Outline each blood parasite and name the species.
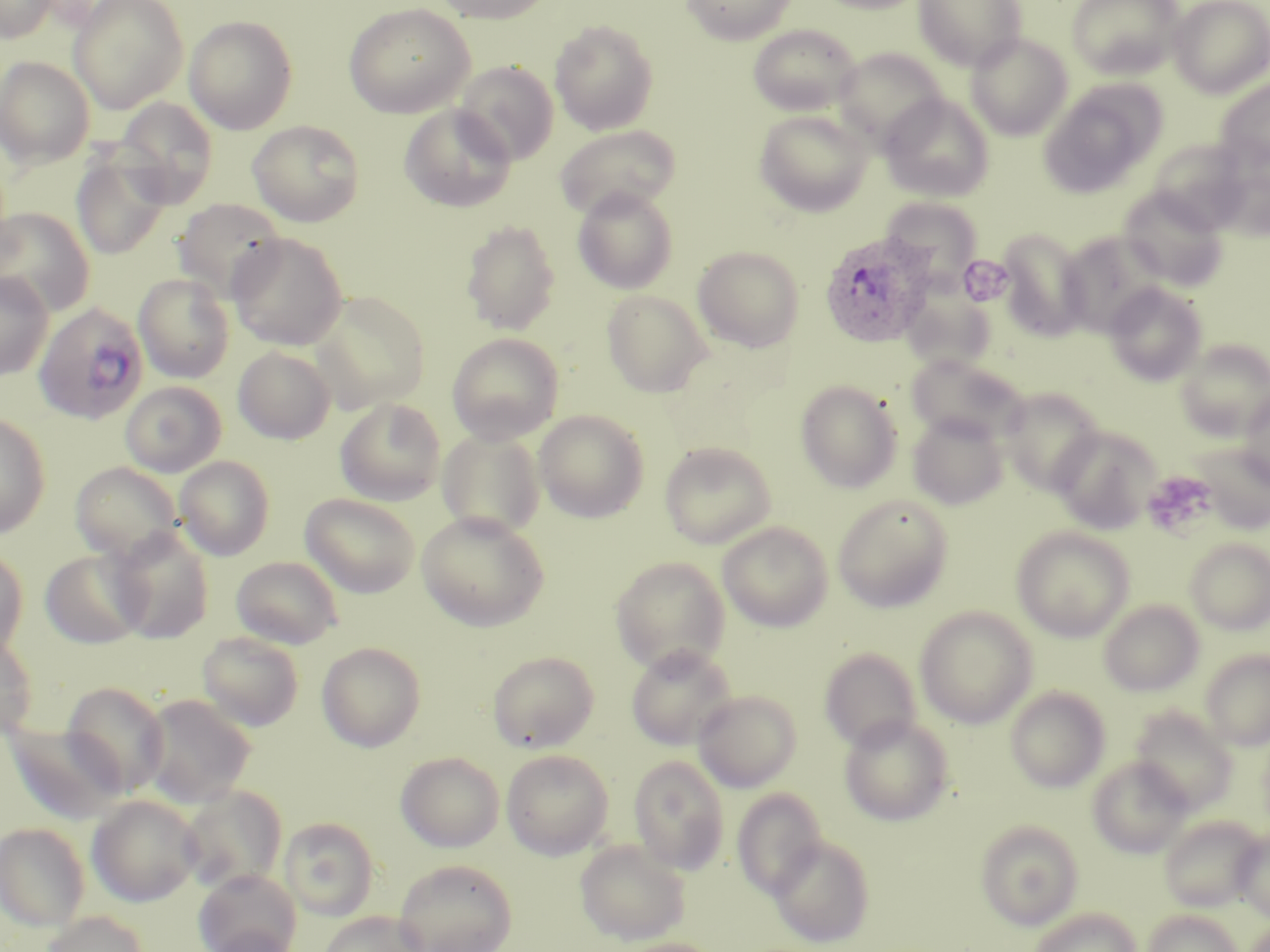

Approximate bounding boxes as (x1, y1, x2, y2) in pixels.
Plasmodium ovale-infected red blood cells: (819, 231, 934, 348), (33, 302, 149, 425).
No Plasmodium falciparum, Plasmodium malariae, Plasmodium vivax, Babesia divergens, or Trypanosoma brucei observed.

Summary:
  - Uninfected red blood cell locations: (0, 0, 57, 42), (69, 0, 188, 113), (432, 0, 557, 25), (680, 0, 797, 45), (812, 0, 930, 14), (912, 0, 1028, 71), (1066, 0, 1184, 81), (1168, 0, 1270, 97), (342, 2, 475, 119), (183, 15, 298, 134), (549, 20, 658, 135), (747, 24, 862, 117), (965, 32, 1073, 140), (834, 47, 949, 151), (0, 56, 95, 167), (454, 61, 559, 165), (1214, 78, 1270, 175), (1040, 81, 1164, 197), (879, 93, 994, 202), (115, 97, 218, 207), (399, 104, 516, 212), (753, 107, 875, 217), (247, 120, 364, 227), (554, 124, 681, 220), (72, 153, 171, 259), (1213, 156, 1270, 241), (572, 186, 679, 294), (1118, 186, 1228, 290), (891, 195, 991, 301), (173, 198, 286, 301), (0, 207, 95, 316), (461, 219, 560, 336), (997, 227, 1091, 341), (1057, 231, 1166, 337), (228, 232, 348, 351), (692, 245, 805, 352), (0, 272, 53, 380), (134, 273, 235, 383), (902, 275, 999, 370), (1104, 282, 1207, 386), (602, 289, 713, 398), (310, 291, 430, 412), (447, 332, 564, 444), (1176, 339, 1270, 441), (233, 345, 335, 444), (906, 353, 1025, 444), (795, 379, 903, 493), (998, 388, 1104, 495), (1238, 391, 1270, 489), (335, 397, 446, 505), (533, 410, 649, 522), (0, 412, 50, 538), (907, 412, 1009, 509), (1051, 425, 1160, 534), (437, 428, 545, 538), (658, 441, 776, 549), (1189, 441, 1270, 534), (175, 455, 274, 560), (70, 461, 182, 561), (300, 493, 420, 597), (832, 493, 953, 613), (417, 511, 550, 631), (717, 521, 833, 631), (108, 527, 214, 644), (1012, 527, 1134, 641), (1184, 539, 1270, 635), (0, 545, 29, 660), (40, 548, 148, 649), (610, 555, 731, 674), (230, 556, 343, 649), (1098, 599, 1204, 696), (915, 606, 1038, 728), (0, 631, 37, 740), (197, 632, 304, 732), (317, 641, 426, 752), (626, 644, 736, 750), (819, 648, 922, 752), (1200, 649, 1270, 750), (488, 651, 599, 753), (61, 681, 170, 798), (1005, 686, 1110, 792), (692, 689, 802, 792), (139, 693, 256, 808), (1129, 706, 1237, 814), (839, 714, 954, 826), (4, 721, 128, 825), (501, 749, 614, 859), (395, 751, 505, 853), (628, 755, 729, 874), (1087, 756, 1193, 858), (178, 785, 287, 894), (732, 789, 827, 898), (87, 794, 201, 907), (1159, 814, 1266, 912), (279, 817, 379, 920), (975, 820, 1083, 929), (1, 822, 91, 930), (1232, 832, 1270, 921), (768, 835, 875, 948), (575, 839, 690, 946), (393, 858, 518, 952), (194, 868, 301, 952), (1028, 907, 1141, 952), (1142, 908, 1243, 952), (39, 911, 149, 952), (319, 911, 427, 952), (205, 927, 301, 952), (609, 937, 722, 952)
  - Platelet locations: (965, 256, 1017, 304), (1142, 469, 1217, 539)
  - Slide-level diagnosis: Plasmodium ovale
  - Field of view: single
  - Modality: optical microscopy
  - Image size: 1270×952 pixels
  - Stain: May-Grünwald-Giemsa
  - Magnification: 1000x
  - Preparation: thin blood film